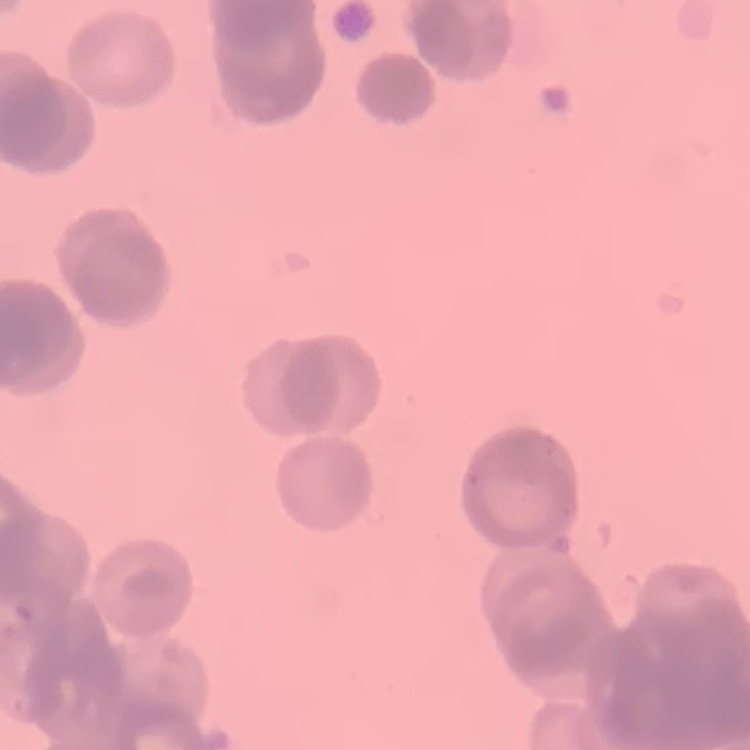

{
  "erythrocyte_morphology": "rouleaux formation",
  "image_type": "square crop of a larger photomicrograph",
  "preparation": "thin peripheral smear",
  "stain": "Field's or Giemsa"
}